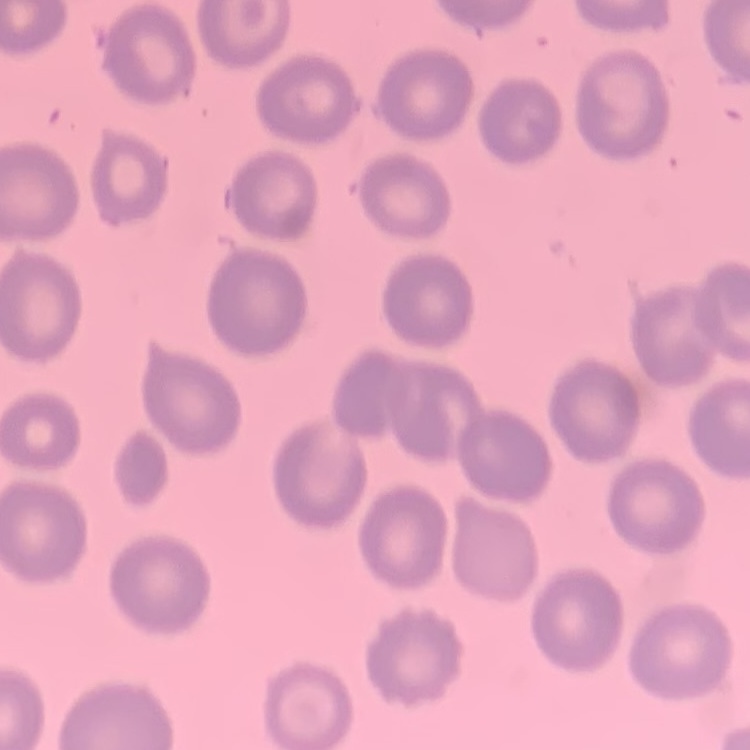

erythrocyte morphology = no rouleaux formation
image type = one tile cut from a larger photomicrograph
preparation = thin blood film
stain = Field's or Giemsa